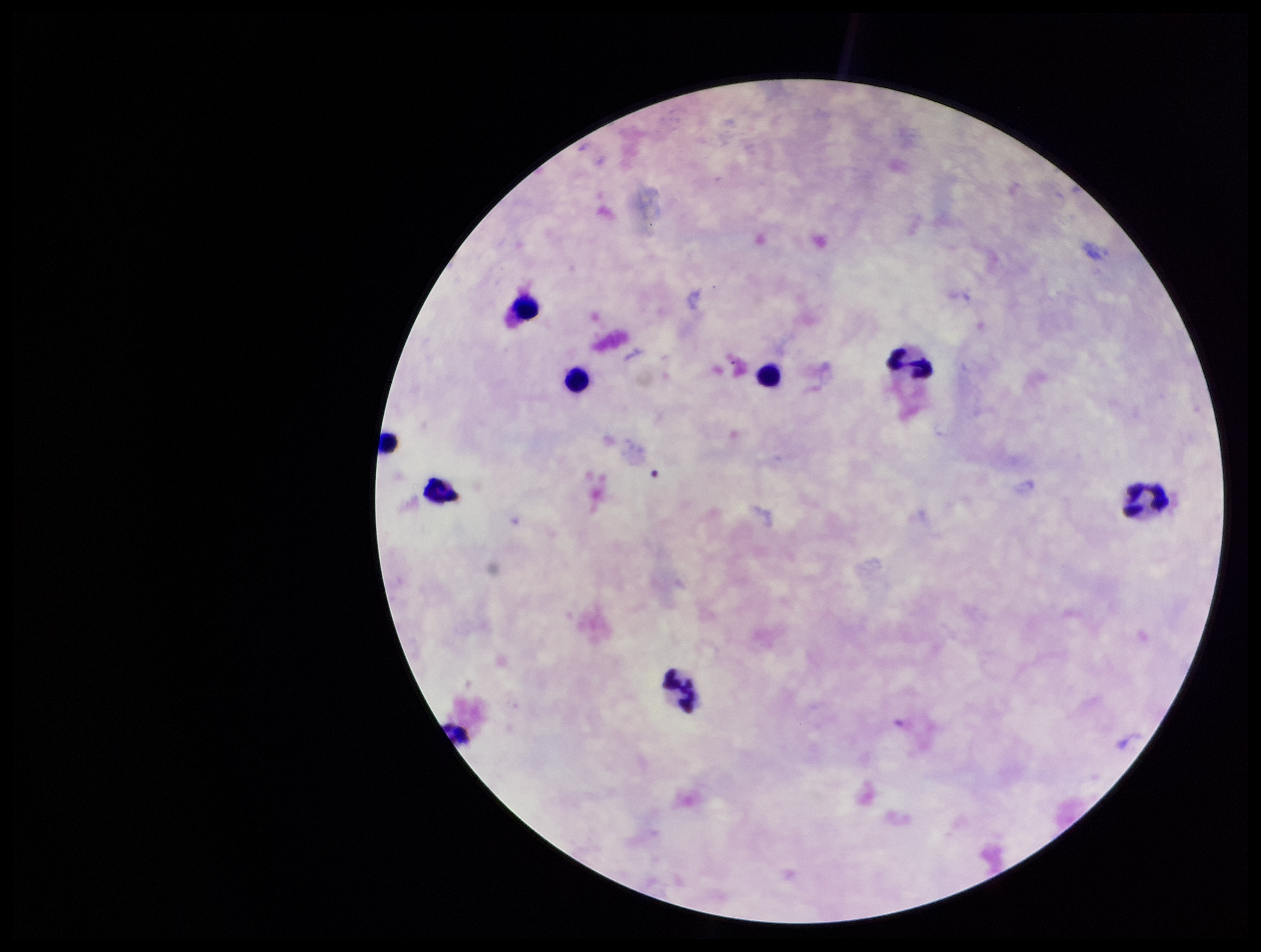

Patient malaria status: negative. Preparation: thick. One field from this slide. Parasite count: 0. Image is 1261×952 pixels. Leukocyte count: 8. Plasmodium parasites: none identified. Smartphone photograph taken through the eyepiece of a microscope. Stained with Giemsa.